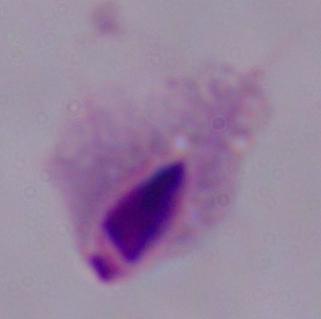

Micrograph. A trichomonad is seen. 1000x magnification.